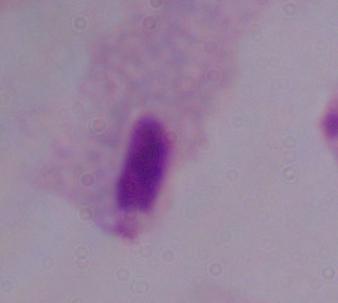
modality = micrograph
identification = trichomonad
magnification = 1000x